Identify the preparation type.
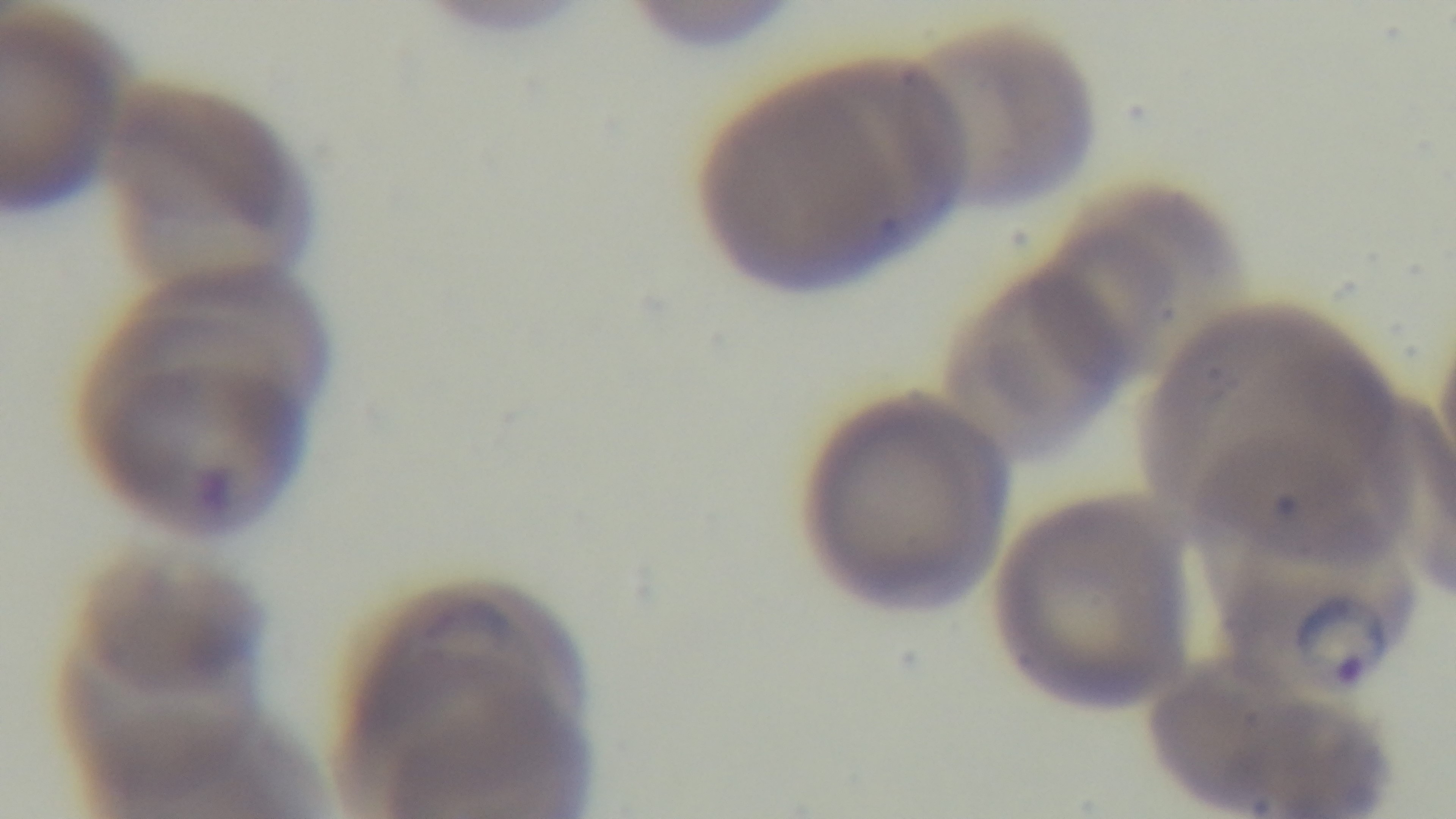
Thin.

Giemsa stain. Light microscopy. Mounted 4K digital camera. One field from the slide. Malaria status: infected. 100x oil-immersion objective.